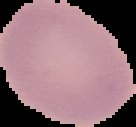
{
  "preparation": "thin blood film",
  "image_size": "136×127 pixels",
  "image_type": "segmented cell region with the area outside set to black",
  "result": "no Plasmodium parasites seen"
}